Assess this cell for malaria.
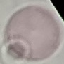

It is uninfected.

Thin blood film. Acquired by smartphone through the microscope eyepiece. Automatically extracted cell patch, resized to 64 × 64 pixels. Giemsa stain.